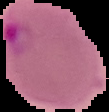

Summary:
  - Image size: 109×112 pixels
  - Preparation: thin blood smear
  - Result: Plasmodium parasites detected
  - Image type: cell region segmented out of the field of view; surrounding area masked to black